Report the malaria status of this cell.
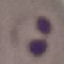
It is parasitized.

stain = Giemsa
image type = automatically extracted cell patch, resized to 64 × 64 pixels
preparation = thin smear
capture = smartphone through the microscope eyepiece